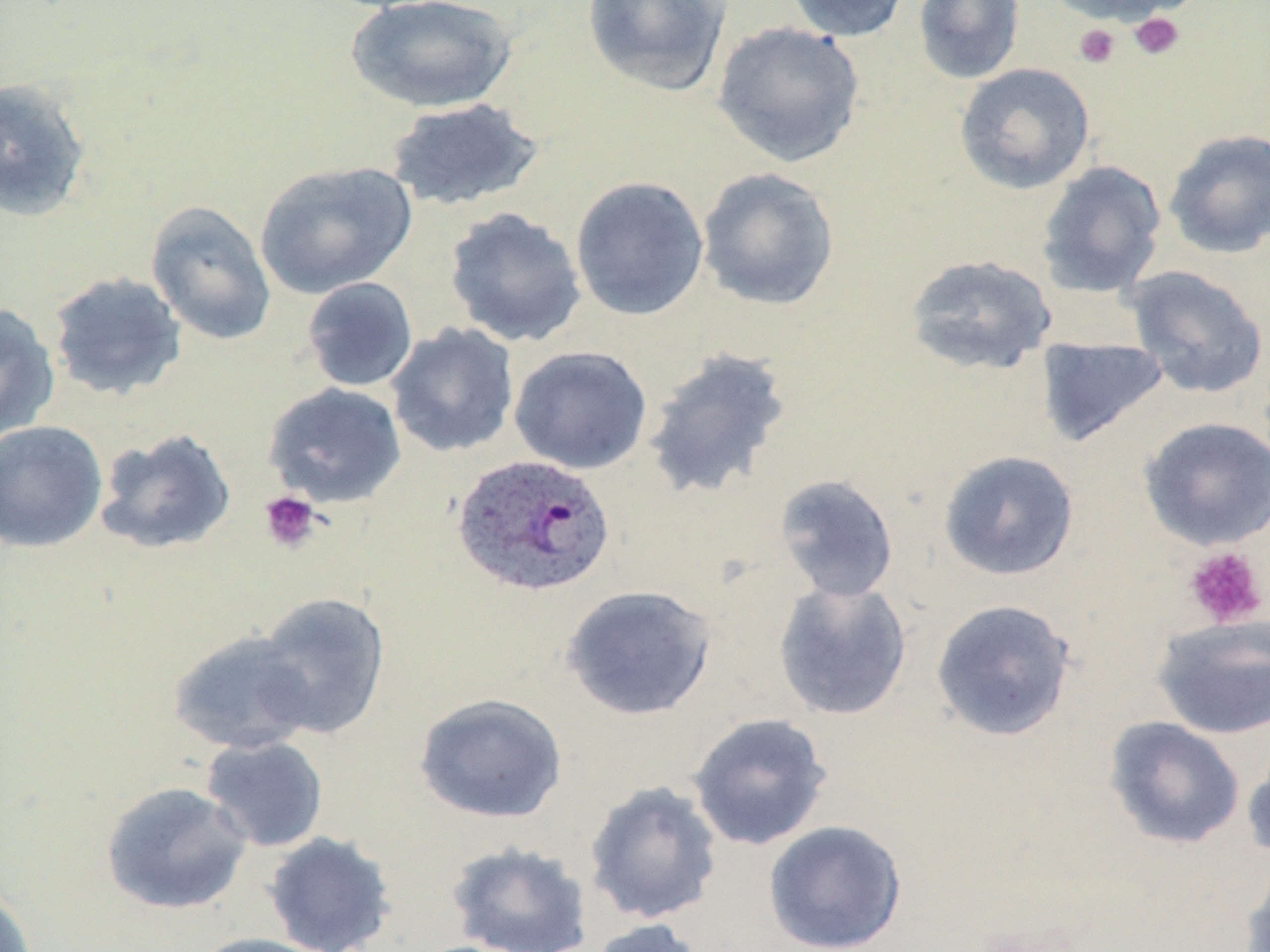
Approximate bounding boxes as named x1/y1/x2/y2 corners in pixels. Platelet locations: (x1=1128, y1=12, x2=1185, y2=61), (x1=1073, y1=24, x2=1121, y2=69), (x1=259, y1=491, x2=322, y2=553), (x1=1182, y1=545, x2=1269, y2=629). Plasmodium ovale-infected red blood cell locations: (x1=453, y1=454, x2=615, y2=597). Uninfected red blood cell locations: (x1=783, y1=0, x2=913, y2=42), (x1=913, y1=0, x2=1026, y2=85), (x1=1041, y1=0, x2=1190, y2=27), (x1=345, y1=1, x2=519, y2=113), (x1=581, y1=1, x2=732, y2=97), (x1=712, y1=21, x2=867, y2=168), (x1=954, y1=62, x2=1096, y2=194), (x1=0, y1=77, x2=92, y2=222), (x1=385, y1=98, x2=545, y2=212), (x1=1163, y1=127, x2=1270, y2=259), (x1=254, y1=160, x2=416, y2=299), (x1=1036, y1=160, x2=1167, y2=299), (x1=696, y1=167, x2=841, y2=311), (x1=569, y1=176, x2=709, y2=322), (x1=145, y1=200, x2=277, y2=345), (x1=443, y1=207, x2=587, y2=348), (x1=904, y1=253, x2=1058, y2=377), (x1=1125, y1=265, x2=1269, y2=399), (x1=47, y1=271, x2=188, y2=401), (x1=301, y1=277, x2=418, y2=392), (x1=0, y1=303, x2=61, y2=442), (x1=386, y1=322, x2=520, y2=458), (x1=1036, y1=335, x2=1170, y2=448), (x1=509, y1=345, x2=653, y2=474), (x1=642, y1=346, x2=794, y2=501), (x1=263, y1=382, x2=407, y2=508), (x1=1138, y1=416, x2=1270, y2=550), (x1=0, y1=420, x2=108, y2=553), (x1=94, y1=427, x2=237, y2=555), (x1=937, y1=449, x2=1081, y2=581), (x1=773, y1=474, x2=900, y2=603), (x1=773, y1=578, x2=913, y2=720), (x1=561, y1=584, x2=717, y2=721), (x1=254, y1=591, x2=390, y2=739), (x1=930, y1=598, x2=1077, y2=742), (x1=1151, y1=614, x2=1270, y2=740), (x1=168, y1=629, x2=318, y2=755), (x1=414, y1=692, x2=569, y2=825), (x1=687, y1=713, x2=833, y2=850), (x1=1104, y1=716, x2=1246, y2=850), (x1=200, y1=736, x2=329, y2=853), (x1=1241, y1=741, x2=1270, y2=865), (x1=583, y1=780, x2=724, y2=925), (x1=99, y1=781, x2=252, y2=916), (x1=763, y1=820, x2=908, y2=952), (x1=263, y1=831, x2=397, y2=952), (x1=446, y1=840, x2=593, y2=952), (x1=1240, y1=860, x2=1270, y2=952), (x1=0, y1=884, x2=38, y2=952), (x1=584, y1=918, x2=711, y2=952), (x1=190, y1=933, x2=333, y2=952). Slide-level diagnosis: Plasmodium ovale. One field of a larger specimen. May-Grünwald-Giemsa stain. Thin blood smear. Light microscopy. Captured at 1000x magnification. Image is 1270×952 pixels.